Comment on the morphology of the erythrocytes.
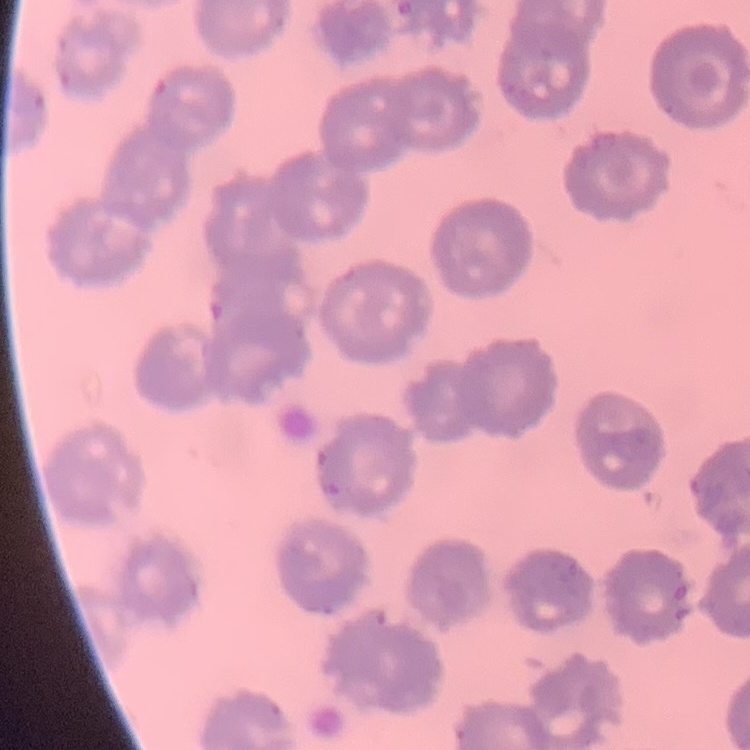
No rouleaux formation.

stain = Field's or Giemsa
preparation = thin blood smear
image type = square crop of a larger photomicrograph